Locate every parasitized red blood cell.
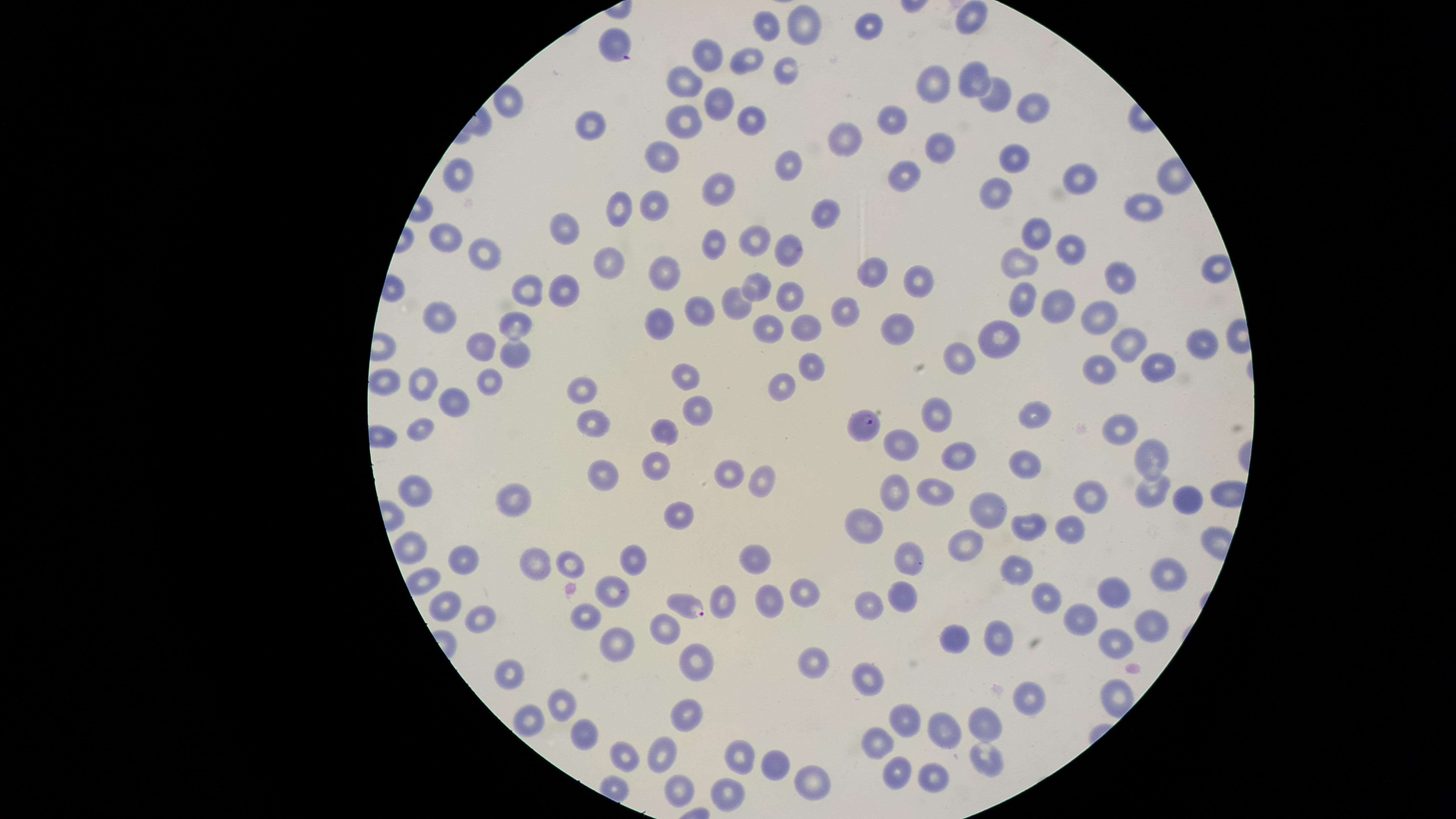

Approximate marker points as {x, y} in pixels.
Parasitized red blood cells: {613, 46}, {861, 424}, {691, 606}.

Approximate marker points as {x, y} in pixels.
Summary:
  - Uninfected red blood cells: {972, 19}, {776, 23}, {804, 24}, {871, 29}, {706, 52}, {746, 60}, {782, 65}, {686, 79}, {974, 79}, {932, 86}, {996, 95}, {718, 100}, {510, 103}, {1032, 106}, {747, 117}, {895, 119}, {685, 120}, {588, 126}, {842, 137}, {942, 150}, {664, 156}, {1016, 160}, {791, 162}, {461, 172}, {907, 175}, {1077, 178}, {719, 184}, {997, 193}, {627, 204}, {1145, 204}, {654, 205}, {828, 214}, {568, 223}, {1032, 233}, {714, 238}, {437, 240}, {757, 241}, {790, 247}, {1069, 247}, {477, 257}, {609, 263}, {1020, 265}, {1218, 269}, {664, 274}, {879, 275}, {1120, 279}, {919, 281}, {755, 286}, {568, 287}, {532, 289}, {794, 295}, {1018, 302}, {736, 303}, {1058, 309}, {690, 313}, {846, 315}, {434, 316}, {1102, 316}, {656, 323}, {514, 324}, {764, 325}, {798, 329}, {1002, 331}, {900, 332}, {1205, 342}, {1126, 344}, {479, 348}, {514, 354}, {967, 357}, {810, 364}, {1158, 366}, {1101, 368}, {685, 378}, {491, 380}, {786, 383}, {382, 384}, {420, 384}, {581, 389}, {455, 404}, {701, 409}, {1036, 412}, {942, 418}, {592, 421}, {1123, 425}, {422, 426}, {665, 426}, {900, 440}, {955, 454}, {1154, 454}, {657, 458}, {1024, 464}, {604, 470}, {733, 471}, {763, 479}, {1152, 487}, {414, 490}, {893, 491}, {937, 491}, {1089, 492}, {518, 495}, {1183, 499}, {988, 506}, {677, 515}, {866, 523}, {1028, 526}, {1069, 529}, {964, 543}, {410, 547}, {632, 557}, {533, 559}, {568, 559}, {751, 559}, {464, 560}, {909, 560}, {1016, 567}, {1169, 572}, {805, 588}, {612, 589}, {904, 589}, {1112, 593}, {1046, 595}, {725, 598}, {768, 598}, {874, 598}, {443, 601}, {584, 616}, {480, 620}, {1081, 620}, {1152, 624}, {669, 630}, {996, 634}, {951, 641}, {612, 643}, {1111, 645}, {700, 658}, {814, 665}, {869, 675}, {511, 676}, {1030, 692}, {563, 706}, {685, 716}, {526, 721}, {900, 721}, {986, 721}, {945, 732}, {587, 737}, {879, 742}, {662, 753}, {620, 757}, {738, 757}, {988, 757}, {778, 765}, {894, 775}, {935, 775}, {810, 778}, {679, 790}, {731, 793}
  - Visible region: circular
  - Species: Plasmodium falciparum
  - Preparation: thin blood film
  - Image size: 1456×819 pixels
  - Field of view: single
  - Stain: Giemsa
  - Capture: smartphone photograph through the microscope eyepiece